Name the parasite shown.
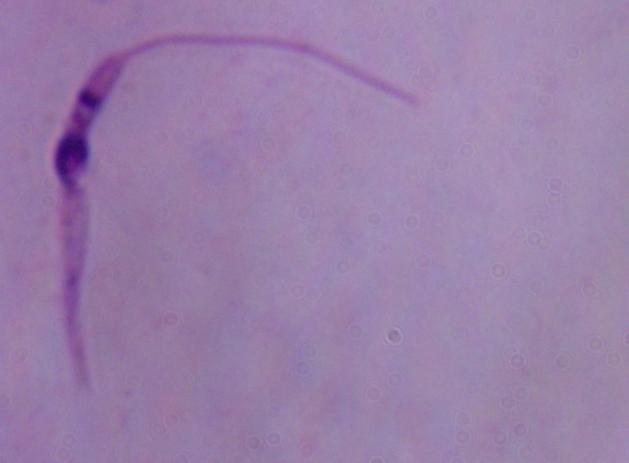
Leishmania.

{
  "modality": "photomicrograph",
  "magnification": "1000x"
}